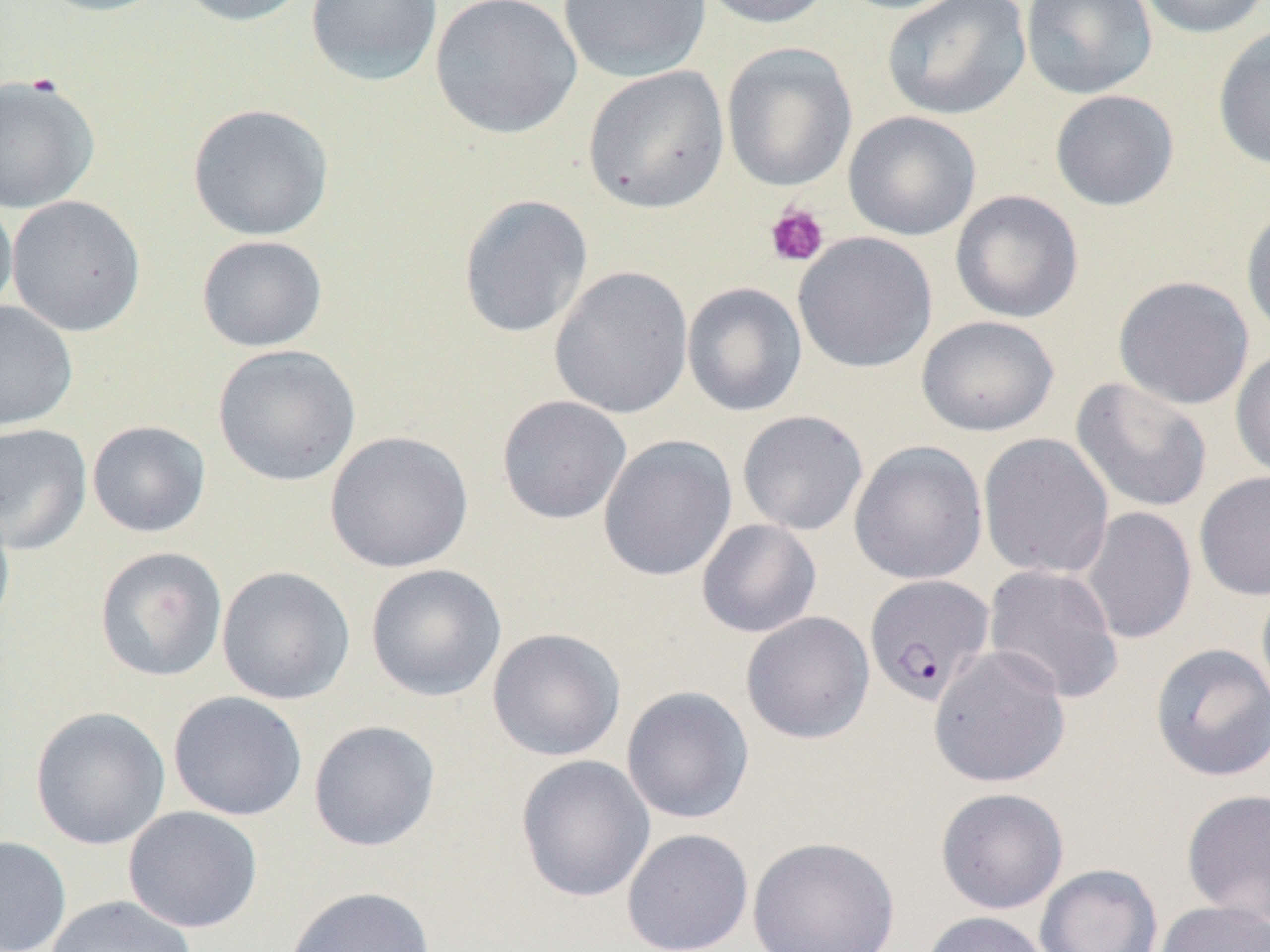
slide-level diagnosis = Plasmodium falciparum
field of view = one of a larger specimen
platelet locations = approximate bounding boxes as named x1/y1/x2/y2 corners in pixels: (x1=764, y1=202, x2=829, y2=268)
image size = 1270×952 pixels
Plasmodium falciparum-infected red blood cell locations = approximate bounding boxes as named x1/y1/x2/y2 corners in pixels: (x1=864, y1=573, x2=995, y2=706)
uninfected red blood cell locations = approximate bounding boxes as named x1/y1/x2/y2 corners in pixels: (x1=31, y1=0, x2=174, y2=17), (x1=175, y1=0, x2=314, y2=27), (x1=305, y1=0, x2=443, y2=86), (x1=429, y1=0, x2=582, y2=139), (x1=558, y1=0, x2=711, y2=83), (x1=693, y1=0, x2=835, y2=29), (x1=831, y1=0, x2=970, y2=15), (x1=882, y1=0, x2=1031, y2=121), (x1=1019, y1=0, x2=1158, y2=100), (x1=1136, y1=0, x2=1268, y2=38), (x1=1212, y1=25, x2=1270, y2=172), (x1=721, y1=42, x2=857, y2=192), (x1=583, y1=65, x2=729, y2=214), (x1=0, y1=74, x2=100, y2=214), (x1=1049, y1=89, x2=1180, y2=211), (x1=187, y1=103, x2=334, y2=241), (x1=843, y1=110, x2=982, y2=242), (x1=950, y1=190, x2=1084, y2=324), (x1=0, y1=191, x2=17, y2=324), (x1=458, y1=194, x2=594, y2=339), (x1=6, y1=195, x2=146, y2=337), (x1=1240, y1=204, x2=1270, y2=343), (x1=792, y1=231, x2=937, y2=374), (x1=196, y1=235, x2=328, y2=353), (x1=549, y1=265, x2=693, y2=420), (x1=1113, y1=275, x2=1255, y2=410), (x1=682, y1=282, x2=807, y2=417), (x1=0, y1=300, x2=79, y2=432), (x1=916, y1=315, x2=1060, y2=437), (x1=212, y1=344, x2=362, y2=487), (x1=1230, y1=346, x2=1270, y2=483), (x1=1070, y1=377, x2=1213, y2=514), (x1=496, y1=395, x2=632, y2=525), (x1=737, y1=410, x2=869, y2=536), (x1=87, y1=420, x2=211, y2=538), (x1=0, y1=423, x2=93, y2=555), (x1=324, y1=430, x2=474, y2=573), (x1=978, y1=433, x2=1115, y2=579), (x1=597, y1=434, x2=738, y2=582), (x1=848, y1=440, x2=988, y2=585), (x1=1193, y1=470, x2=1270, y2=600), (x1=0, y1=497, x2=16, y2=638), (x1=1077, y1=506, x2=1198, y2=645), (x1=696, y1=518, x2=822, y2=638), (x1=94, y1=546, x2=228, y2=682), (x1=365, y1=563, x2=507, y2=701), (x1=983, y1=564, x2=1124, y2=705), (x1=216, y1=565, x2=356, y2=705), (x1=1255, y1=579, x2=1270, y2=713), (x1=741, y1=611, x2=875, y2=744), (x1=487, y1=627, x2=626, y2=762), (x1=1149, y1=643, x2=1270, y2=783), (x1=928, y1=645, x2=1071, y2=789), (x1=621, y1=686, x2=755, y2=824), (x1=168, y1=691, x2=308, y2=822), (x1=29, y1=706, x2=171, y2=850), (x1=308, y1=719, x2=441, y2=852), (x1=514, y1=754, x2=656, y2=903), (x1=935, y1=787, x2=1069, y2=915), (x1=1180, y1=788, x2=1270, y2=924), (x1=123, y1=805, x2=263, y2=933), (x1=621, y1=828, x2=754, y2=952), (x1=746, y1=835, x2=901, y2=952), (x1=0, y1=836, x2=71, y2=951), (x1=1035, y1=863, x2=1163, y2=952), (x1=283, y1=885, x2=437, y2=952), (x1=44, y1=895, x2=197, y2=952), (x1=1154, y1=900, x2=1270, y2=952), (x1=917, y1=911, x2=1053, y2=952)
magnification = 1000x
preparation = thin blood smear
modality = light microscopy